Name the blood parasite species.
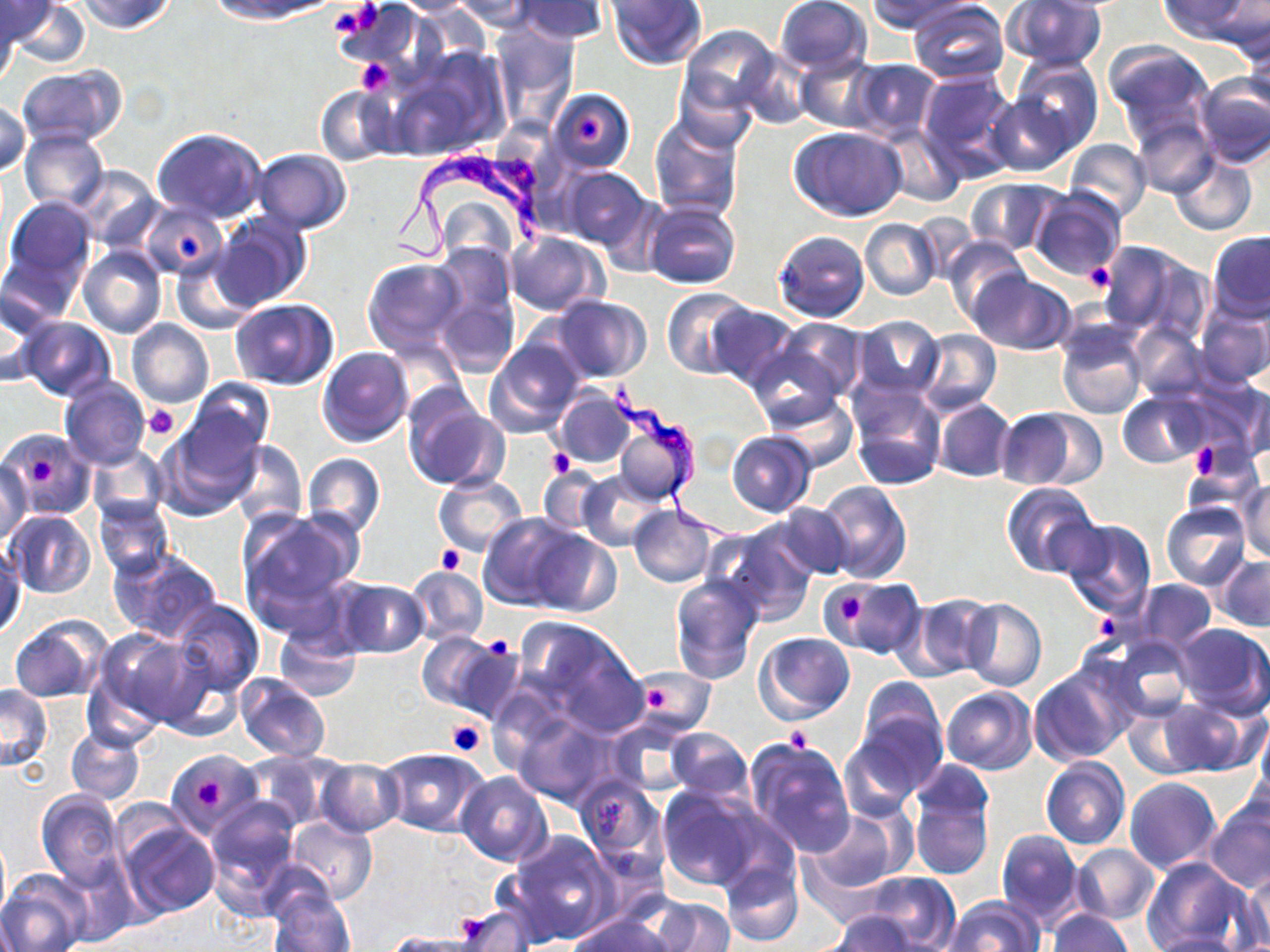

Trypanosoma brucei.

Approximate bounding boxes as (x1, y1, x2, y2) in pixels. Trypanosoma brucei locations: (388, 143, 552, 263), (612, 378, 751, 547). Uninfected red blood cell locations: (80, 0, 174, 35), (210, 0, 339, 22), (389, 0, 487, 15), (450, 0, 540, 32), (515, 0, 607, 43), (606, 0, 708, 70), (772, 0, 873, 77), (869, 0, 971, 32), (1159, 0, 1255, 45), (1211, 0, 1270, 59), (0, 1, 58, 46), (9, 1, 90, 70), (908, 1, 1008, 85), (1004, 1, 1107, 72), (334, 2, 426, 80), (0, 6, 20, 86), (679, 25, 783, 120), (490, 26, 578, 127), (1243, 31, 1269, 116), (1104, 40, 1215, 141), (390, 49, 506, 160), (735, 50, 812, 130), (1010, 55, 1103, 155), (795, 56, 882, 131), (848, 58, 941, 140), (16, 65, 126, 147), (916, 69, 1019, 181), (1193, 74, 1270, 168), (315, 86, 399, 165), (550, 88, 635, 174), (986, 90, 1075, 175), (0, 100, 30, 178), (1129, 115, 1218, 197), (650, 117, 744, 221), (878, 123, 966, 205), (790, 125, 908, 221), (152, 127, 267, 224), (21, 129, 109, 213), (1062, 137, 1151, 224), (252, 148, 352, 232), (1170, 153, 1257, 235), (72, 166, 161, 251), (556, 167, 652, 253), (964, 178, 1066, 256), (1028, 186, 1126, 282), (5, 196, 96, 290), (645, 201, 742, 290), (139, 202, 228, 279), (212, 213, 310, 311), (861, 219, 941, 300), (505, 230, 607, 316), (774, 230, 869, 323), (1207, 231, 1270, 321), (942, 236, 1028, 324), (1096, 240, 1202, 339), (78, 245, 166, 339), (170, 253, 258, 333), (430, 256, 519, 376), (363, 258, 467, 357), (969, 271, 1076, 355), (0, 288, 54, 387), (663, 288, 754, 377), (547, 296, 652, 383), (229, 299, 337, 390), (1197, 300, 1270, 388), (708, 303, 800, 390), (852, 316, 946, 400), (20, 317, 116, 401), (128, 318, 213, 407), (1056, 319, 1148, 419), (753, 320, 866, 421), (1129, 323, 1209, 402), (916, 328, 1001, 414), (484, 337, 586, 439), (317, 347, 413, 447), (1174, 375, 1269, 460), (60, 377, 149, 470), (185, 378, 273, 467), (1232, 379, 1270, 465), (847, 383, 947, 491), (552, 387, 636, 469), (1117, 391, 1210, 467), (403, 392, 508, 492), (770, 394, 860, 470), (932, 397, 1016, 483), (608, 405, 699, 506), (995, 408, 1087, 490), (157, 422, 259, 518), (5, 430, 95, 518), (726, 431, 816, 517), (228, 437, 307, 529), (1184, 444, 1262, 512), (88, 445, 168, 527), (302, 453, 386, 539), (1, 456, 33, 543), (537, 469, 602, 534), (576, 469, 666, 550), (433, 473, 527, 557), (1236, 479, 1270, 562), (814, 481, 911, 583), (1001, 482, 1100, 579), (94, 497, 174, 580), (1162, 500, 1252, 591), (628, 503, 717, 587), (774, 503, 854, 579), (238, 509, 362, 626), (5, 511, 94, 598), (479, 512, 582, 609), (1054, 518, 1157, 618), (712, 521, 817, 626), (529, 530, 622, 617), (1, 546, 24, 639), (110, 548, 223, 644), (1215, 555, 1270, 632), (405, 565, 488, 646), (670, 573, 766, 684), (332, 576, 429, 658), (822, 576, 924, 656), (1135, 581, 1215, 650), (897, 593, 995, 681), (170, 599, 265, 695), (960, 599, 1046, 691), (8, 615, 107, 703), (513, 616, 646, 734), (1172, 622, 1270, 718), (274, 624, 363, 703), (94, 629, 210, 730), (755, 632, 855, 723), (417, 633, 515, 718), (1098, 634, 1196, 723), (1029, 665, 1132, 766), (632, 670, 714, 734), (82, 672, 165, 753), (234, 674, 329, 763), (856, 677, 946, 773), (0, 684, 53, 770), (941, 686, 1038, 774), (1157, 695, 1262, 777), (1121, 703, 1210, 781), (840, 714, 944, 812), (514, 718, 613, 806), (607, 722, 692, 796), (1249, 724, 1270, 822), (66, 727, 144, 804), (667, 728, 753, 802), (745, 735, 856, 858), (378, 748, 489, 835), (166, 751, 263, 834), (242, 751, 338, 832), (1040, 757, 1130, 849), (317, 759, 404, 836), (457, 772, 552, 867), (575, 776, 668, 874), (1123, 777, 1221, 873), (909, 784, 993, 881), (657, 786, 760, 891), (35, 790, 124, 887), (1205, 797, 1270, 894), (203, 798, 300, 911), (807, 807, 909, 896), (284, 817, 377, 905), (115, 818, 219, 920), (995, 828, 1085, 930), (0, 829, 10, 927), (509, 829, 616, 944), (1073, 843, 1159, 925), (57, 856, 137, 945), (1139, 856, 1252, 952), (721, 860, 804, 947), (1, 868, 90, 951), (1241, 868, 1269, 950), (855, 871, 961, 949), (269, 890, 356, 952), (943, 896, 1044, 952), (645, 897, 736, 951), (452, 903, 534, 951), (823, 911, 926, 952), (1047, 911, 1132, 952), (569, 912, 674, 952), (1143, 932, 1251, 952), (382, 933, 481, 952). Platelet locations: (327, 3, 381, 39), (356, 57, 394, 95), (577, 116, 604, 146), (177, 235, 203, 261), (1083, 262, 1116, 292), (144, 405, 180, 440), (1188, 446, 1219, 479), (546, 448, 573, 477), (24, 453, 55, 482), (436, 546, 463, 573), (837, 591, 867, 626), (1090, 608, 1123, 646), (480, 635, 514, 661), (646, 688, 668, 714), (447, 720, 486, 757), (784, 726, 812, 752), (194, 775, 225, 811). One field of a larger specimen. Light microscopy. 1000x magnification. Image is 1270×952 pixels. Thin blood film. May-Grünwald-Giemsa stain.